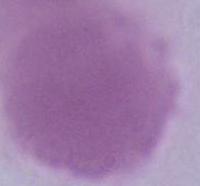

An erythrocyte is shown. Photomicrograph. Captured at 1000x magnification.